Describe the morphology of the erythrocytes.
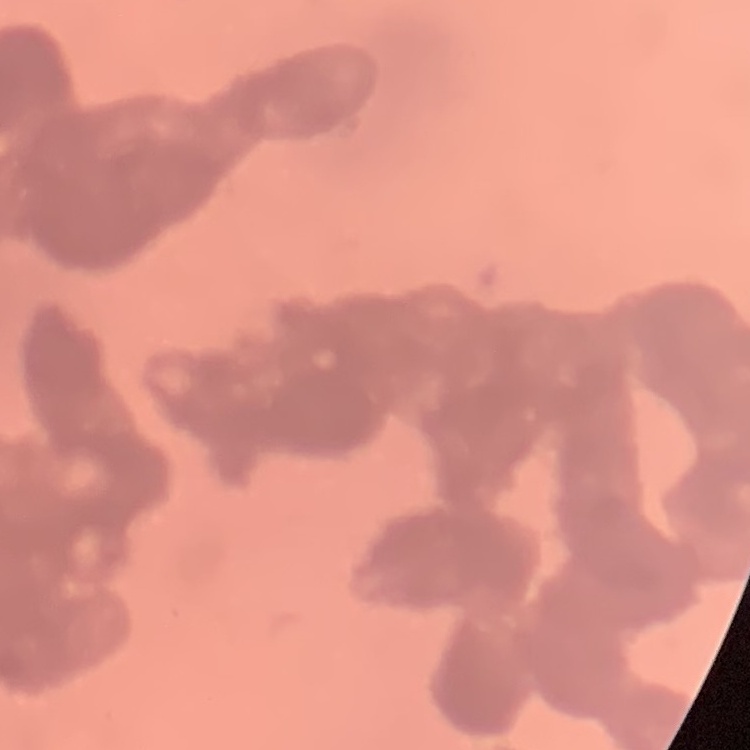
Rouleaux formation.

Summary:
  - Image type: square crop of a larger photomicrograph
  - Preparation: thin peripheral smear
  - Stain: Field's or Giemsa